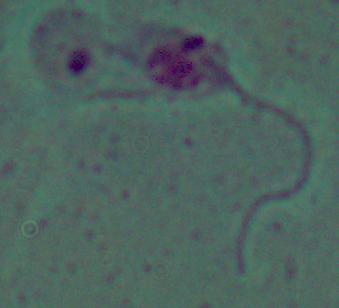
Summary:
  - Modality: photomicrograph
  - Identification: Leishmania
  - Magnification: 1000x